Point out each Plasmodium parasite.
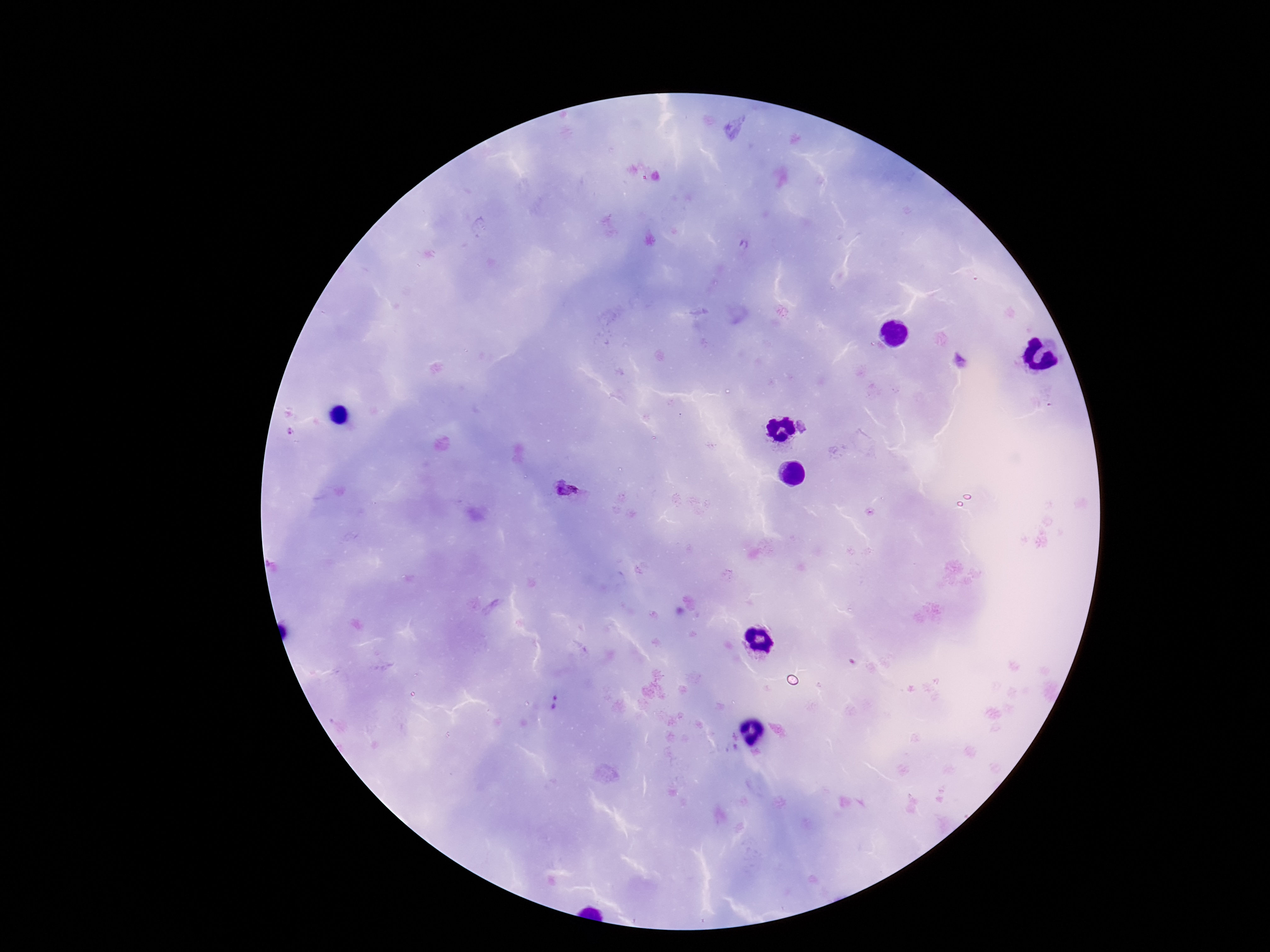
Approximate centers as [x, y] in pixels.
Plasmodium parasites: [806, 427], [567, 489], [554, 703].

capture = smartphone camera through the microscope eyepiece
patient malaria status = infected
field of view = one from this slide
image size = 1270×952 pixels
magnification = 100x
stain = Giemsa
preparation = thick blood smear